State the blood parasite species.
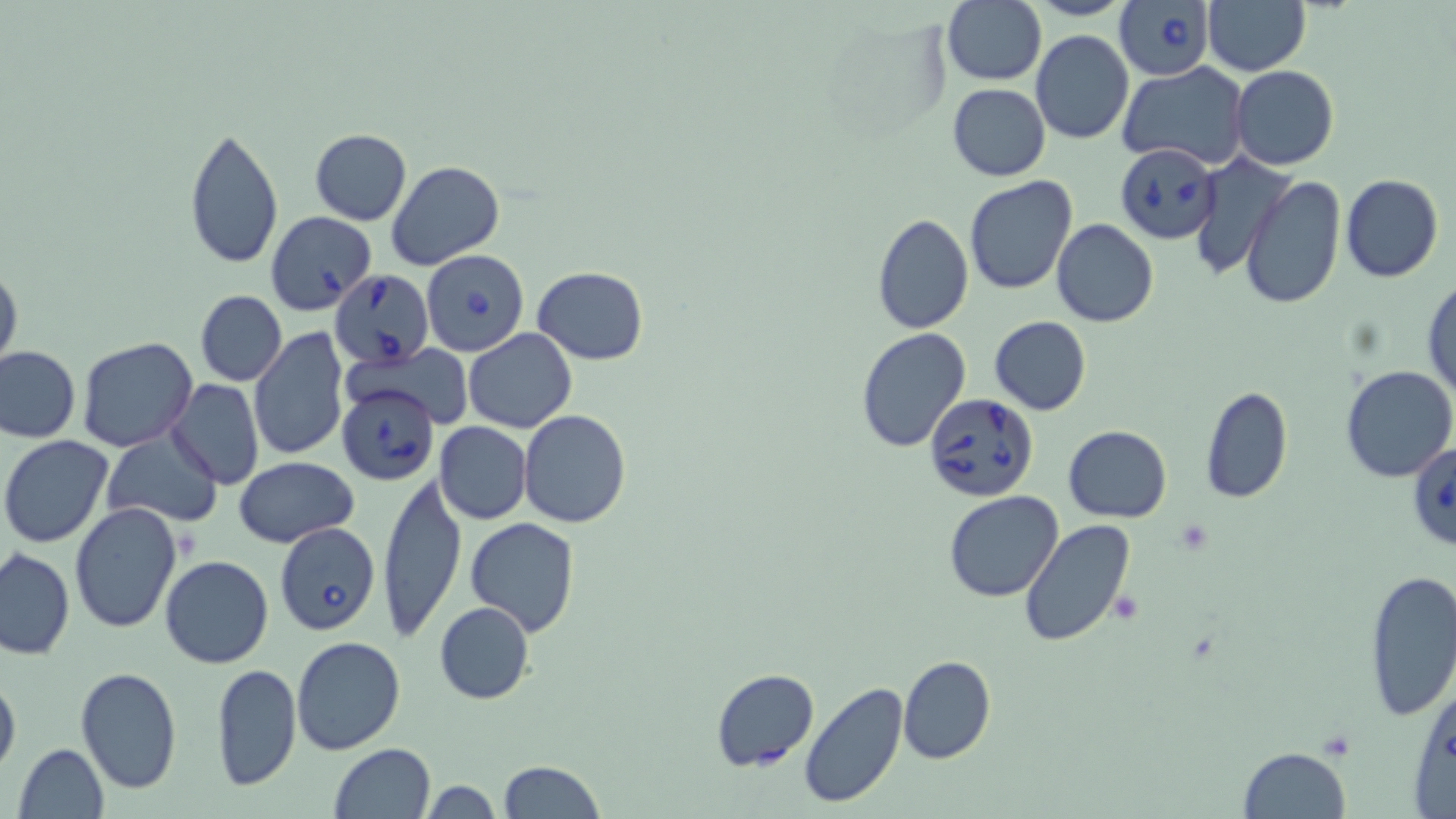

Babesia divergens.

Summary:
  - Coordinate format: approximate bounding boxes as named x1/y1/x2/y2 corners in pixels
  - Babesia divergens-infected red blood cell locations: (x1=1113, y1=0, x2=1214, y2=81), (x1=1117, y1=143, x2=1221, y2=244), (x1=265, y1=212, x2=377, y2=314), (x1=421, y1=248, x2=530, y2=359), (x1=330, y1=270, x2=434, y2=367), (x1=335, y1=383, x2=439, y2=485), (x1=924, y1=392, x2=1042, y2=503), (x1=1407, y1=440, x2=1456, y2=552), (x1=275, y1=523, x2=381, y2=638)
  - Uninfected red blood cell locations: (x1=942, y1=0, x2=1047, y2=86), (x1=1202, y1=0, x2=1311, y2=76), (x1=1030, y1=30, x2=1133, y2=143), (x1=1118, y1=63, x2=1250, y2=169), (x1=1231, y1=65, x2=1339, y2=169), (x1=946, y1=83, x2=1051, y2=181), (x1=183, y1=124, x2=284, y2=270), (x1=309, y1=129, x2=412, y2=226), (x1=1189, y1=154, x2=1292, y2=280), (x1=387, y1=161, x2=503, y2=269), (x1=1340, y1=174, x2=1442, y2=283), (x1=965, y1=175, x2=1077, y2=294), (x1=1240, y1=177, x2=1345, y2=310), (x1=871, y1=213, x2=974, y2=333), (x1=1052, y1=219, x2=1159, y2=327), (x1=0, y1=262, x2=23, y2=375), (x1=533, y1=267, x2=648, y2=364), (x1=1423, y1=277, x2=1456, y2=403), (x1=196, y1=291, x2=287, y2=386), (x1=989, y1=316, x2=1091, y2=414), (x1=248, y1=327, x2=349, y2=464), (x1=463, y1=328, x2=576, y2=432), (x1=854, y1=328, x2=972, y2=452), (x1=77, y1=338, x2=199, y2=452), (x1=358, y1=343, x2=476, y2=428), (x1=0, y1=345, x2=80, y2=443), (x1=1341, y1=363, x2=1456, y2=482), (x1=166, y1=379, x2=264, y2=488), (x1=1200, y1=385, x2=1293, y2=503), (x1=519, y1=410, x2=632, y2=528), (x1=434, y1=422, x2=532, y2=524), (x1=1063, y1=424, x2=1172, y2=524), (x1=101, y1=431, x2=224, y2=527), (x1=1, y1=434, x2=116, y2=548), (x1=233, y1=456, x2=358, y2=547), (x1=377, y1=472, x2=466, y2=643), (x1=944, y1=491, x2=1064, y2=603), (x1=69, y1=502, x2=183, y2=634), (x1=1020, y1=517, x2=1136, y2=647), (x1=465, y1=518, x2=582, y2=637), (x1=1, y1=547, x2=75, y2=660), (x1=160, y1=555, x2=274, y2=669), (x1=1361, y1=568, x2=1456, y2=724), (x1=435, y1=601, x2=535, y2=704), (x1=292, y1=636, x2=407, y2=755), (x1=897, y1=655, x2=997, y2=765), (x1=212, y1=663, x2=300, y2=792), (x1=75, y1=666, x2=183, y2=795), (x1=710, y1=667, x2=819, y2=771), (x1=0, y1=670, x2=21, y2=778), (x1=1409, y1=678, x2=1456, y2=817), (x1=796, y1=681, x2=909, y2=809), (x1=13, y1=742, x2=110, y2=818), (x1=327, y1=743, x2=435, y2=819), (x1=1236, y1=746, x2=1351, y2=819), (x1=499, y1=760, x2=603, y2=819), (x1=419, y1=779, x2=503, y2=818)
  - Field of view: single
  - Modality: optical microscopy
  - Magnification: 1000x
  - Image size: 1456×819 pixels
  - Preparation: thin blood smear
  - Stain: May-Grünwald-Giemsa